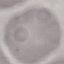

Result: no malaria parasites seen. Automatically extracted cell patch, resized to 64 × 64 pixels. Thin smear of blood. Acquired by smartphone through the microscope eyepiece. Giemsa-stained preparation.